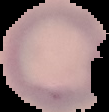 Malaria status: uninfected. From a thin blood film. Segmented cell region on a black background. Image is 109×112 pixels.